Assess the morphology of the red blood cells.
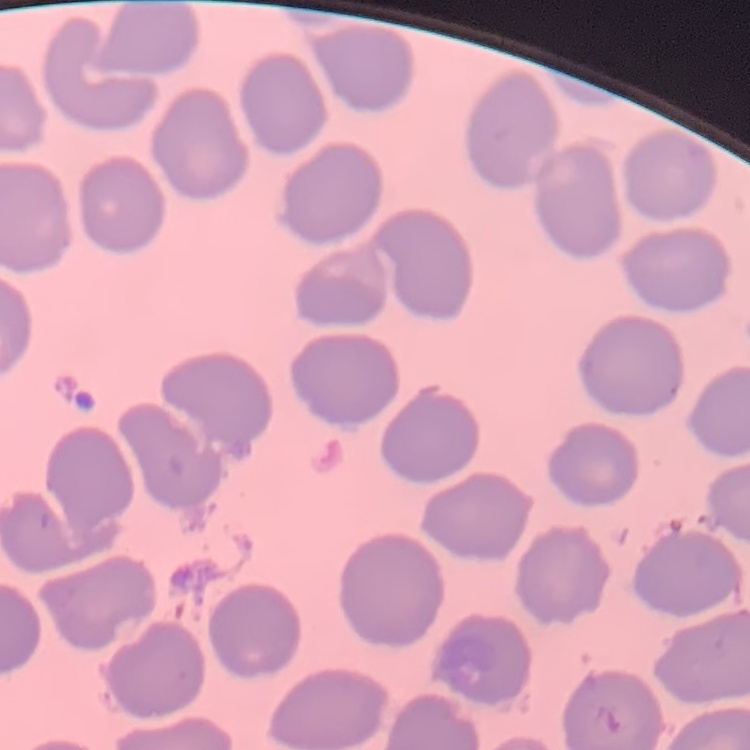
They show no rouleaux formation.

Thin peripheral smear. Field's or Giemsa stain. One tile cut from a larger photomicrograph.